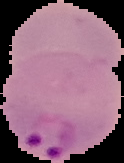

image type = segmented cell region with the area outside set to black
image size = 124×163 pixels
preparation = thin blood film
malaria status = parasitized